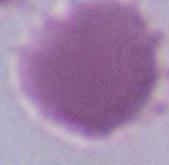
Summary:
  - Identification: red blood cell
  - Modality: photomicrograph
  - Magnification: 1000x